State the preparation type.
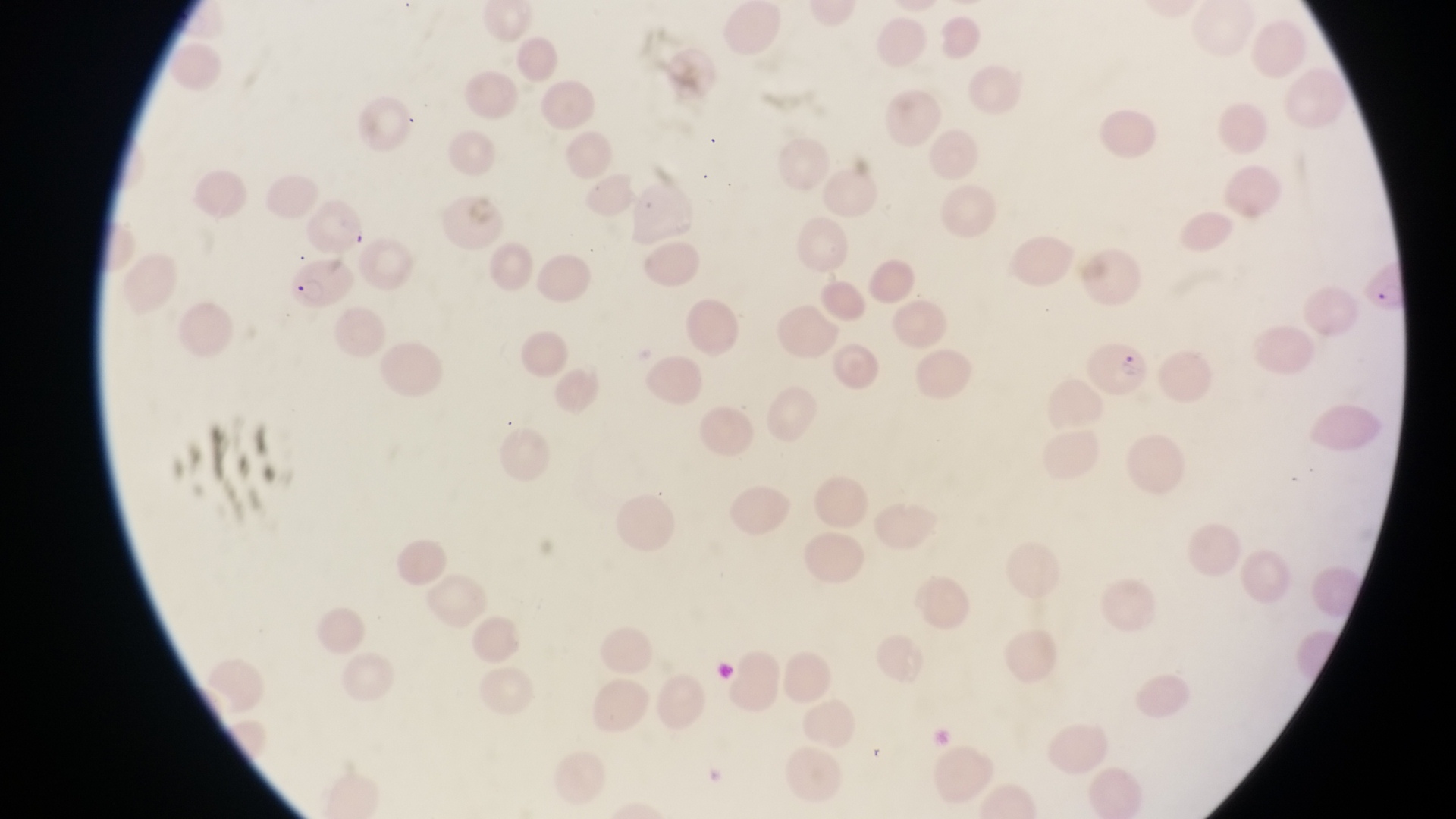
Thin blood film.

country = Uganda
capture = smartphone photograph through the eyepiece of an Olympus CX-23 microscope
image size = 1456×819 pixels
magnification = 1000x
parasitised red blood cell locations = approximate bounding boxes as left top right bottom in pixels: 285 254 351 313; 1360 257 1409 318; 1083 334 1149 401
field of view = single